Comment on the morphology of the erythrocytes.
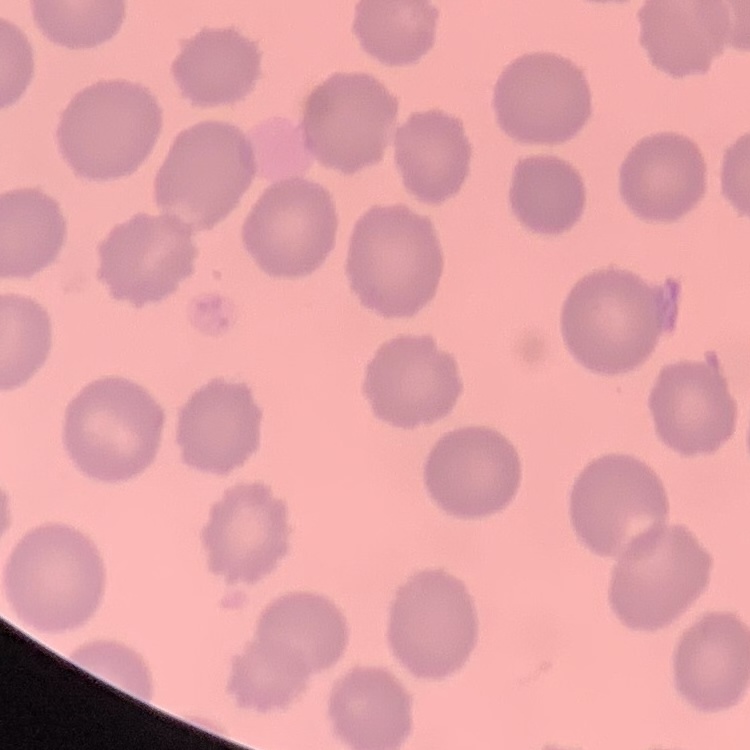
No rouleaux formation.

Summary:
  - Stain: Field's or Giemsa
  - Preparation: thin blood smear
  - Image type: one tile cut from a larger photomicrograph